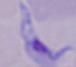

modality: micrograph
magnification: 1000x
identification: trypanosome